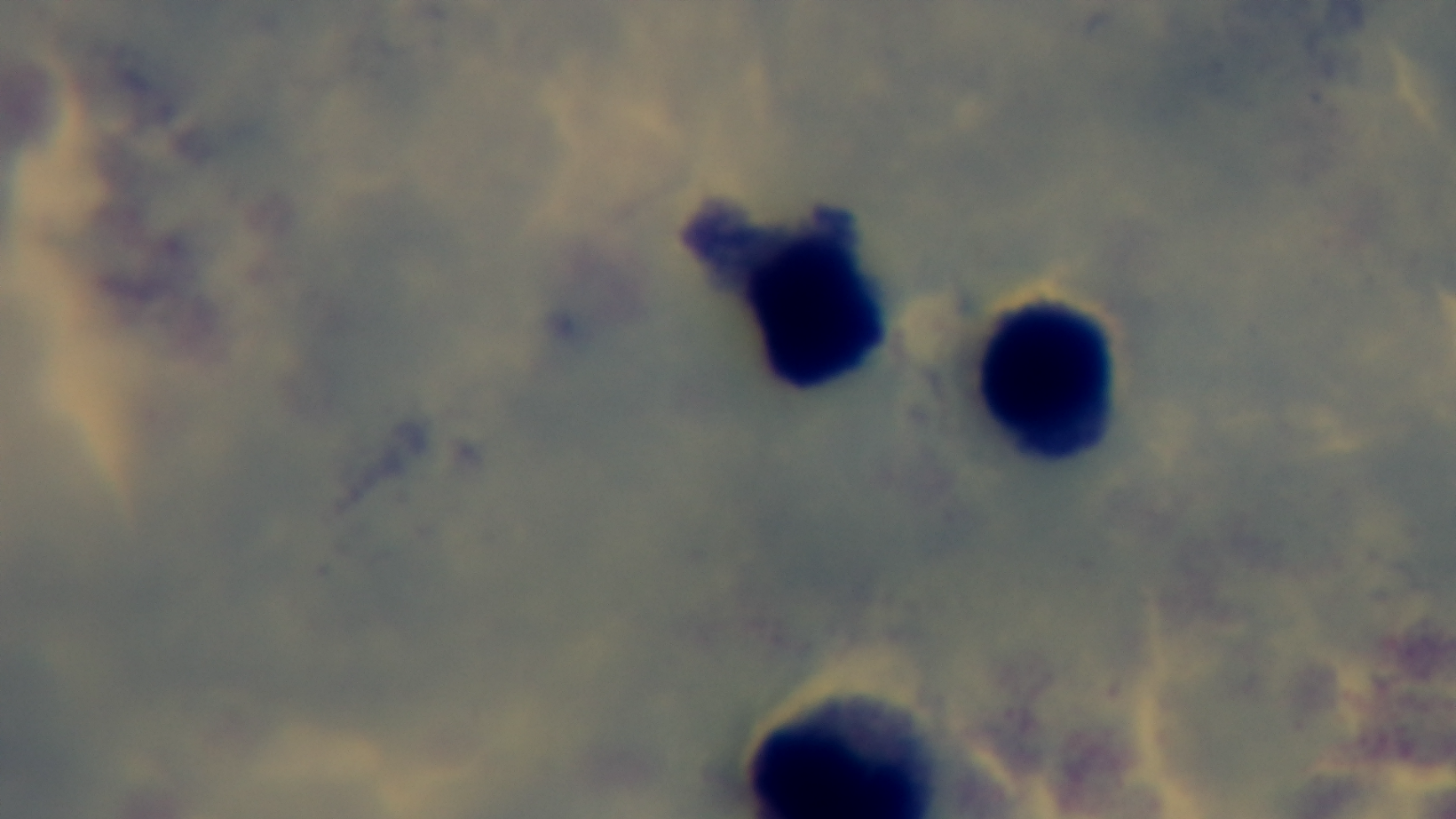

Photomicrograph. Oil-immersion objective, 100x. Captured with a mounted 4K digital camera. Giemsa-stained. Preparation: thick smear. Malaria status: negative. Single field of view.